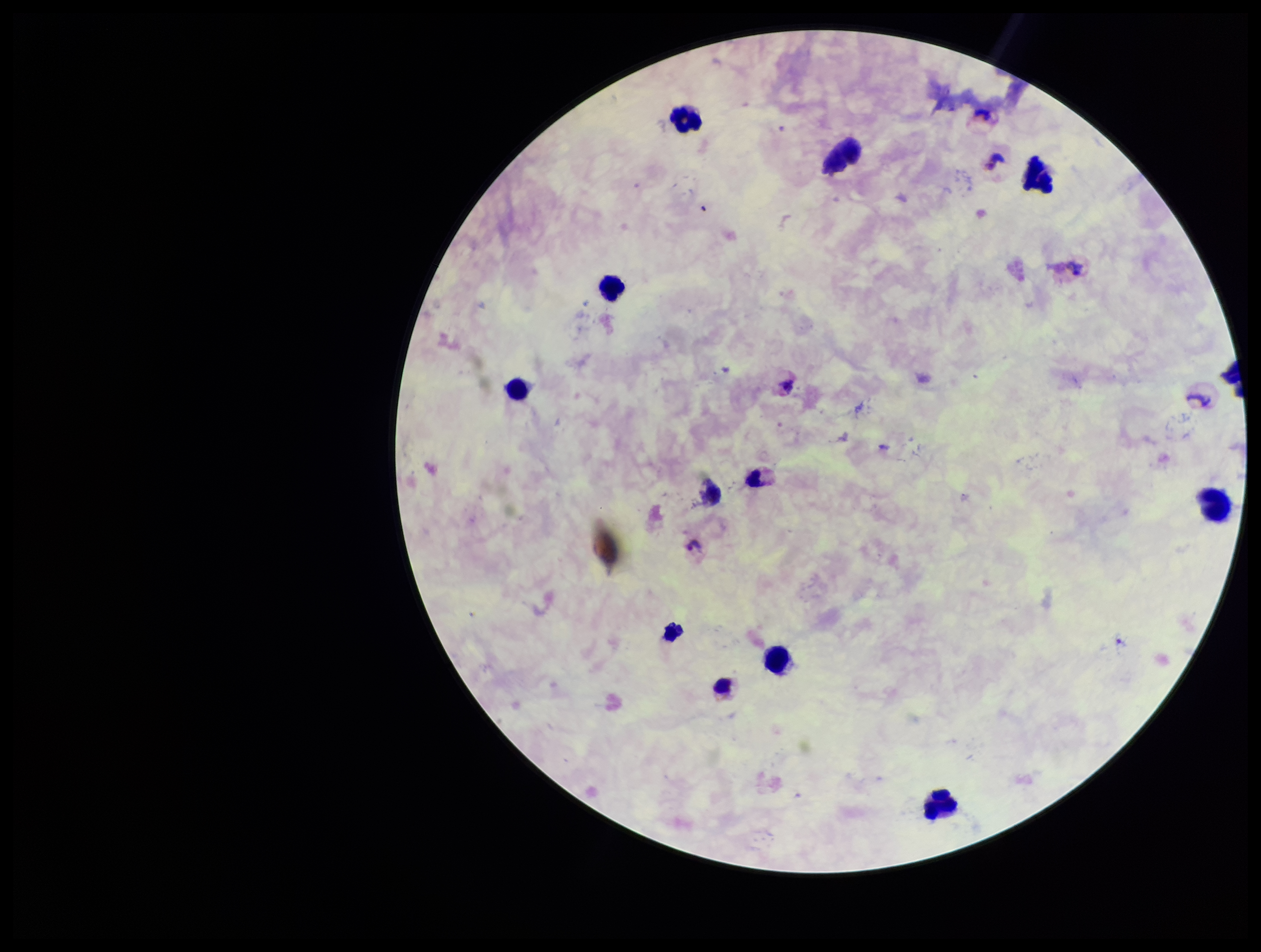
leukocyte count = 12
capture = smartphone photograph through the microscope eyepiece
image size = 1261×952 pixels
preparation = thick blood smear
stain = Giemsa
species reported for this patient = Plasmodium vivax
Plasmodium parasites = detected
patient malaria status = infected
field of view = single
parasite count = 2